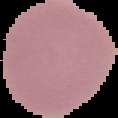

Result: no Plasmodium parasites seen. The area outside the segmented cell region is set to black. Image is 118×118 pixels. From a thin blood smear.